Comment on the morphology of the erythrocytes.
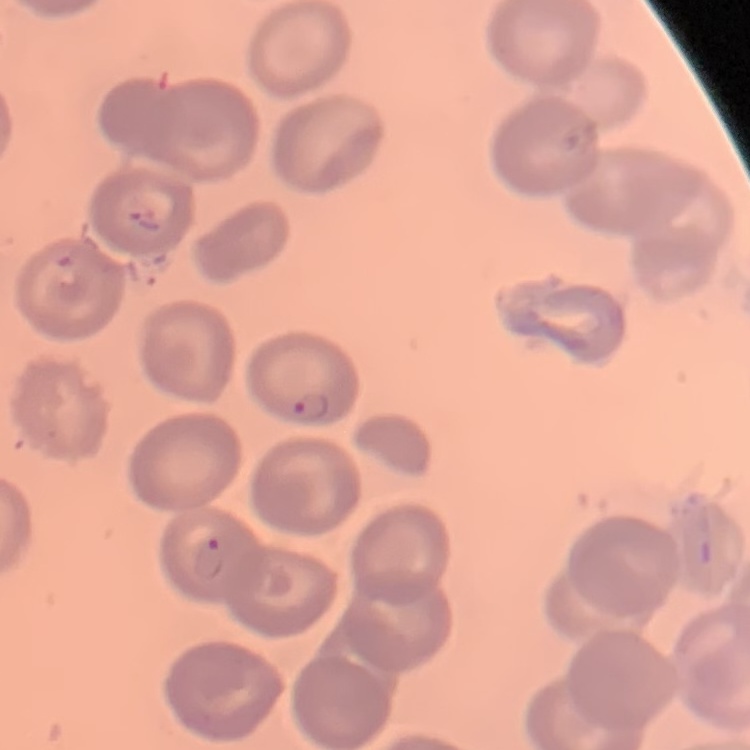

No rouleaux formation.

Summary:
  - Image type: square crop of a larger photomicrograph
  - Preparation: thin blood film
  - Stain: Field's or Giemsa